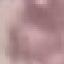

malaria status = uninfected
preparation = thin smear
capture = smartphone through the microscope eyepiece
stain = Giemsa
image type = cell patch, automatically extracted from a larger field of view and resized to 64 × 64 pixels